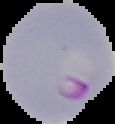
malaria status = parasitized
preparation = thin blood smear
image size = 115×124 pixels
image type = cell region segmented out of the field of view; surrounding area masked to black